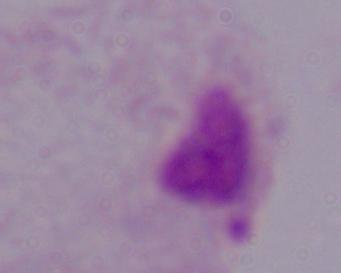

identification = trichomonad
magnification = 1000x
modality = micrograph